Give the position of every malaria parasite.
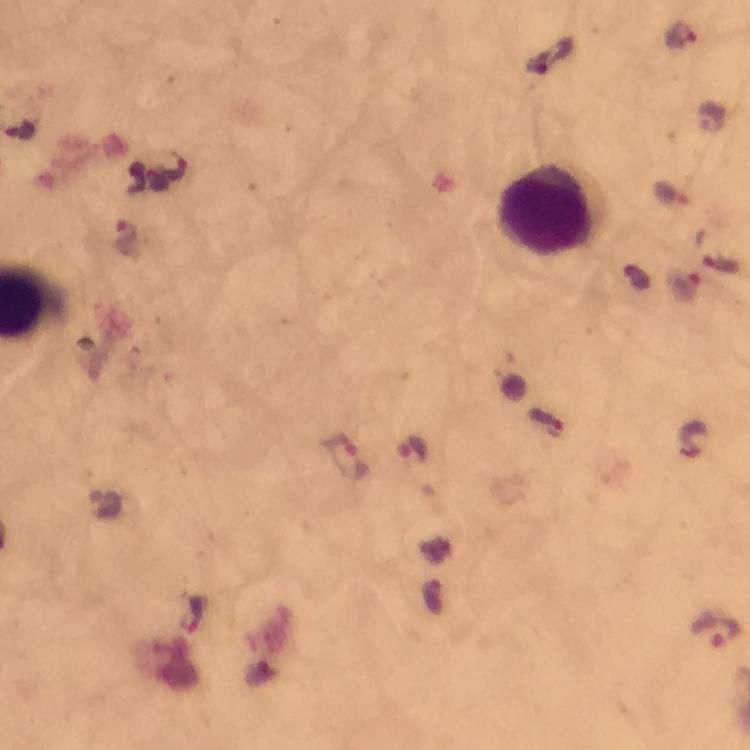
Approximate centers as {x, y} in pixels.
Malaria parasites: {680, 35}, {714, 117}, {20, 130}, {173, 164}, {126, 239}, {683, 284}, {545, 422}, {415, 448}, {348, 457}, {716, 628}.

cropped from = one field of view
stain = Giemsa
magnification = 100x
preparation = thick blood film
immersion oil = applied
image size = 750×750 pixels
capture = smartphone mounted on the microscope
context = from a diagnostic examination for malaria
leukocyte locations = approximate centers as {x, y} in pixels: {548, 209}